Name the parasite shown.
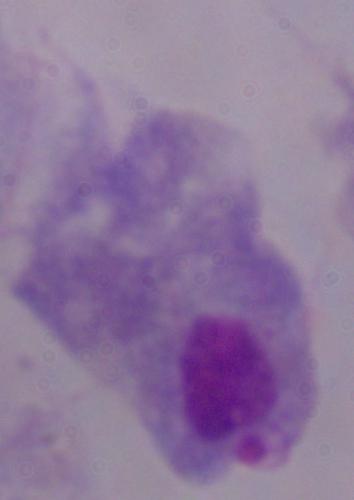
A trichomonad.

Summary:
  - Magnification: 1000x
  - Modality: photomicrograph